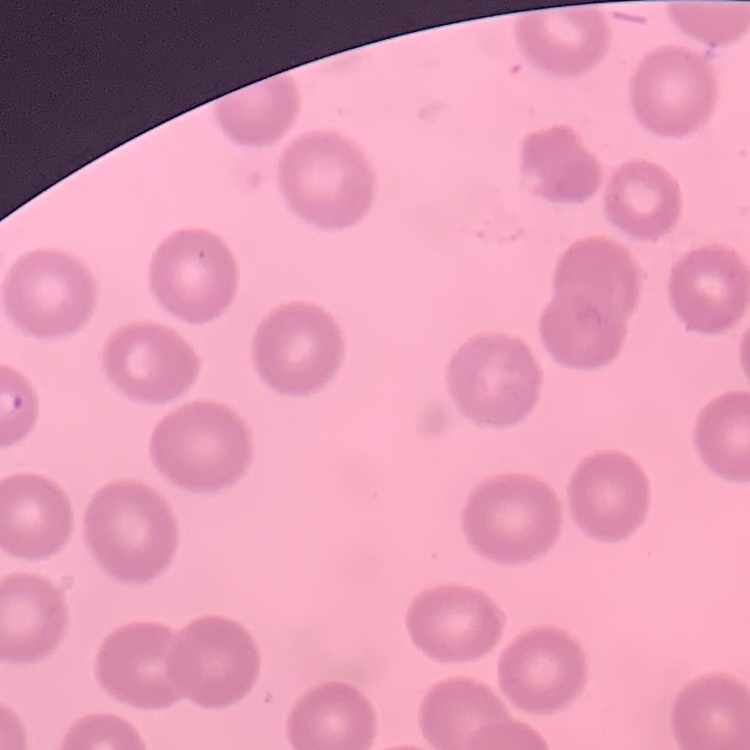
The red blood cells exhibit no rouleaux formation. One tile cut from a larger photomicrograph. Thin peripheral smear. Field's or Giemsa stain.